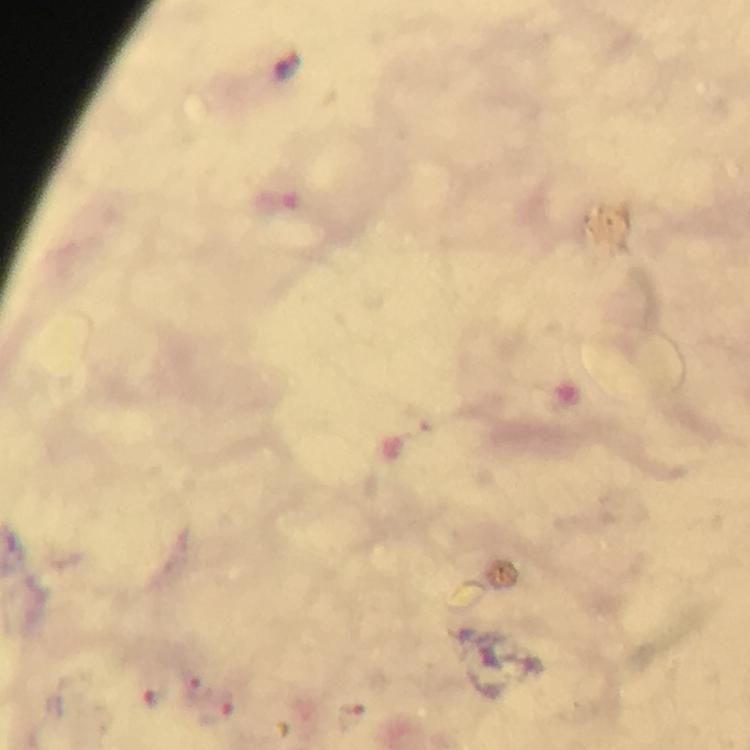

Approximate centers as [x, y] in pixels. Malaria parasite locations: [198, 691], [349, 714]. At 100x magnification. A crop from one field of view. Photographed with a smartphone mounted on the microscope. Thick blood smear. Giemsa stain. Immersion oil applied. From a malaria diagnostic workup. Image is 750×750 pixels.